Point out each Plasmodium parasite.
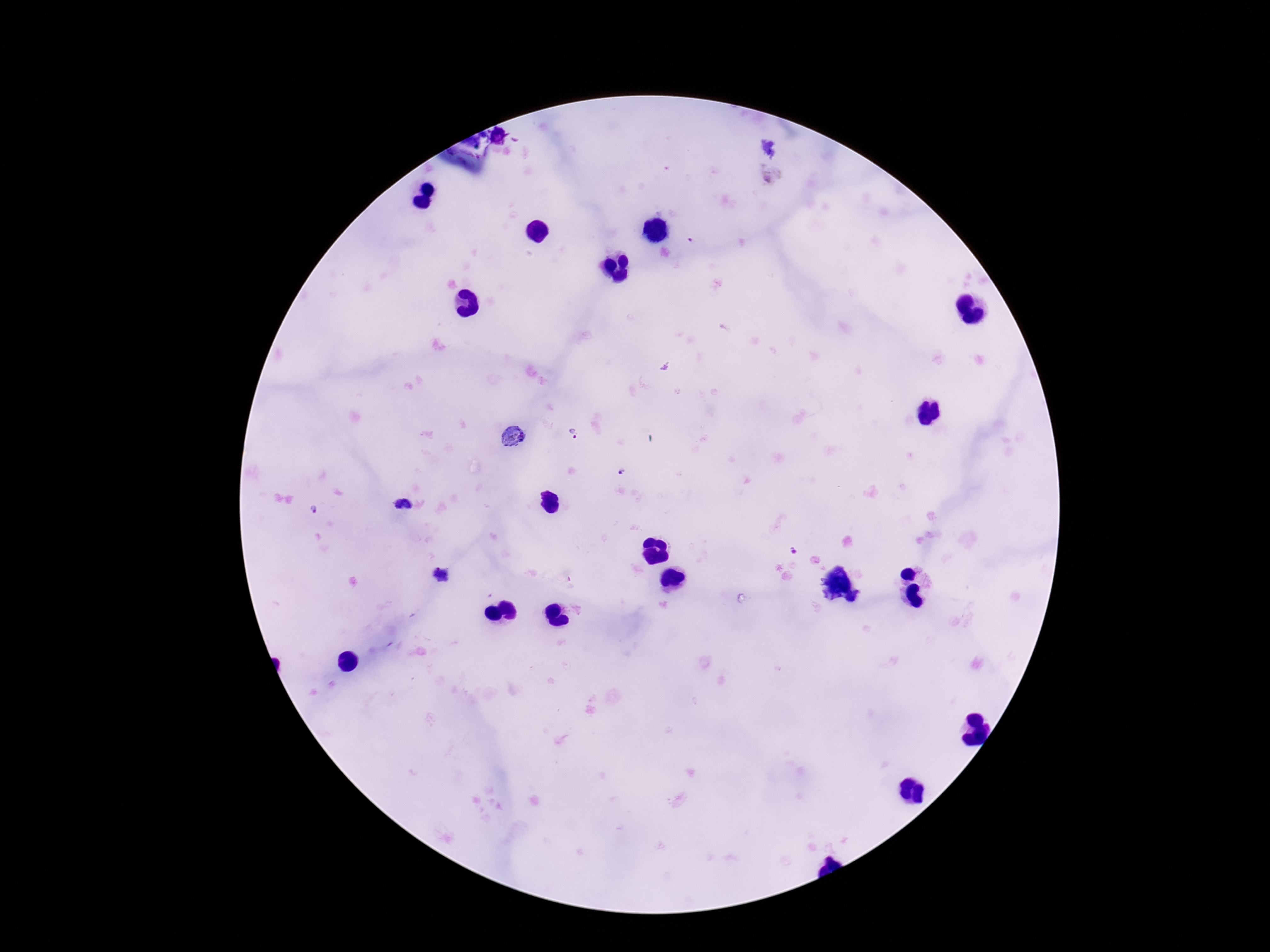
Approximate centers as {x, y} in pixels.
Plasmodium parasites: {574, 434}, {512, 436}, {621, 471}, {316, 509}, {793, 551}, {853, 598}.

Single field of view. Smartphone photograph taken through the microscope eyepiece. Image is 1270×952 pixels. Thick blood smear. 100x magnification. Giemsa-stained preparation. Patient malaria status: infected.